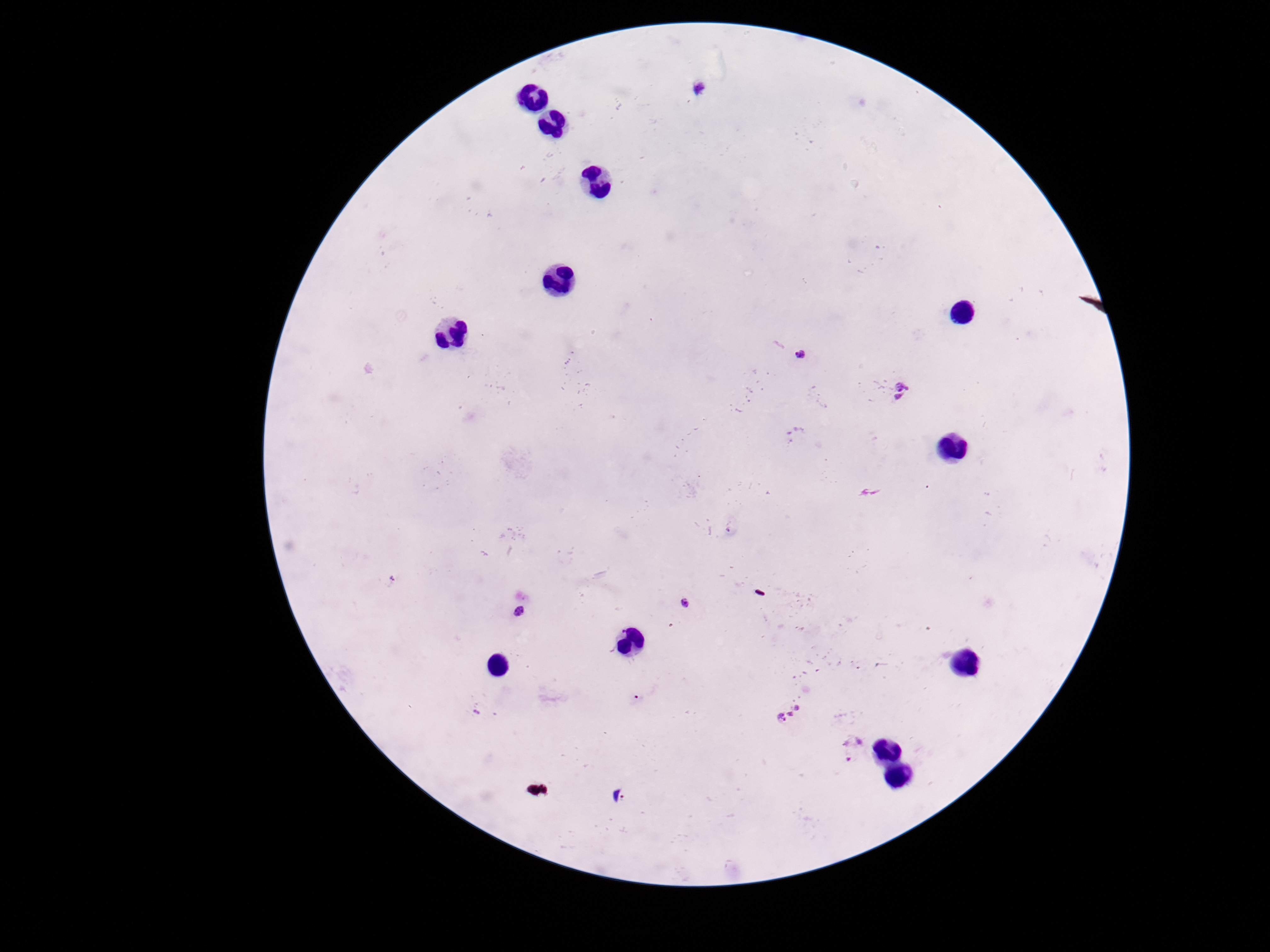

field of view = single
magnification = 100x
capture = smartphone camera through the microscope eyepiece
stain = Giemsa
preparation = thick blood smear
Plasmodium parasite locations = approximate centers as (x, y) in pixels: (699, 88), (803, 356), (898, 391), (684, 603), (519, 612), (795, 712), (850, 748), (621, 796)
patient malaria status = positive
image size = 1270×952 pixels